Report the malaria status of this cell.
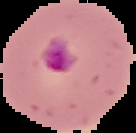

It is parasitized.

{
  "preparation": "thin blood smear",
  "image_type": "cell region segmented out of the field of view; surrounding area masked to black",
  "image_size": "136×133 pixels"
}